Locate every leukocyte (white blood cell).
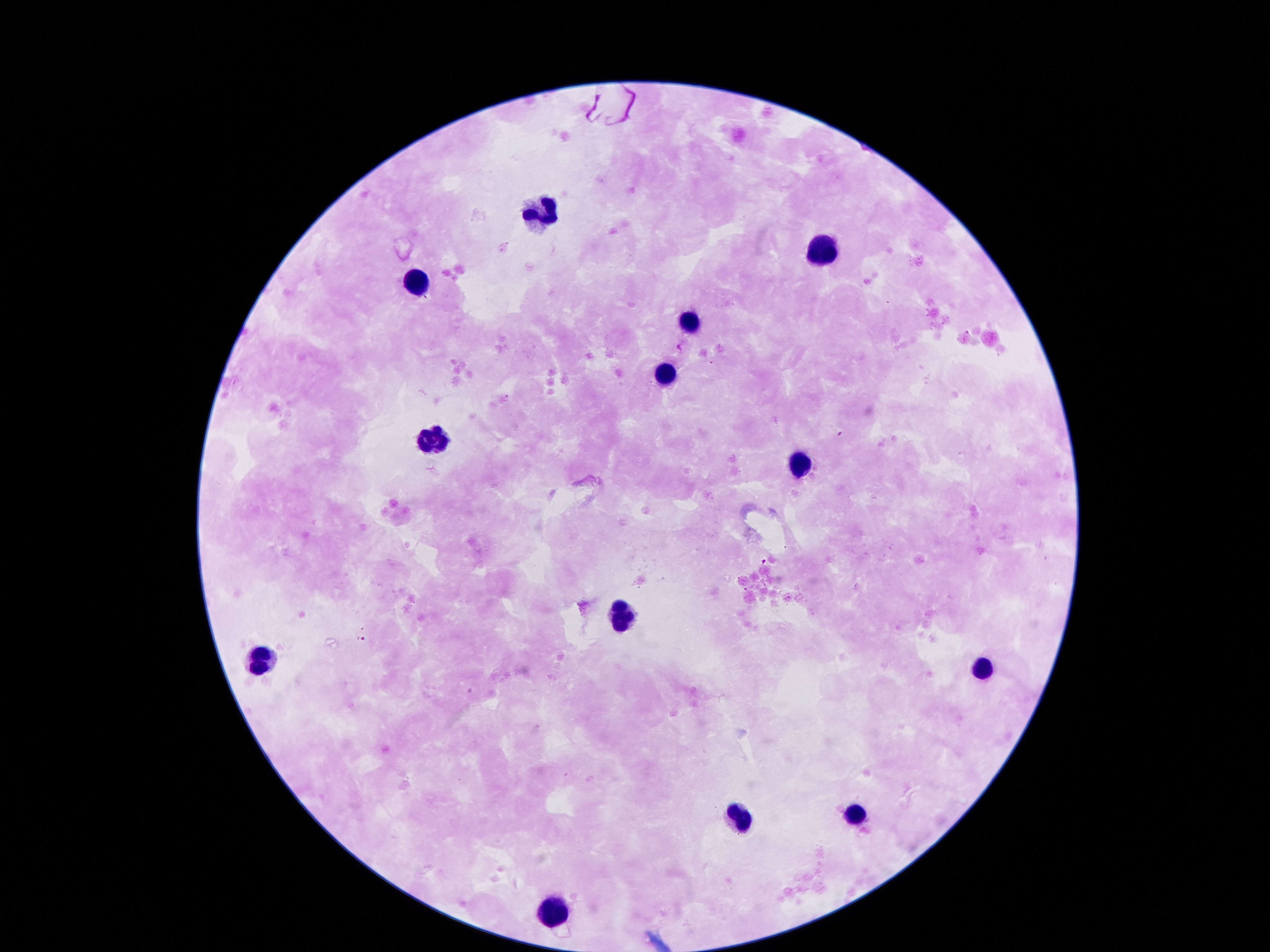
Approximate centers as [x, y] in pixels.
Leukocytes: [539, 209], [820, 243], [409, 289], [687, 316], [668, 374], [432, 437], [804, 461], [619, 615], [267, 657], [985, 671], [855, 812], [739, 816], [552, 912].

Image is 1270×952 pixels. Single field of view. 100x magnification. Smartphone photograph taken through the microscope eyepiece. Patient malaria status: negative. Thick peripheral-blood smear. Giemsa stain.